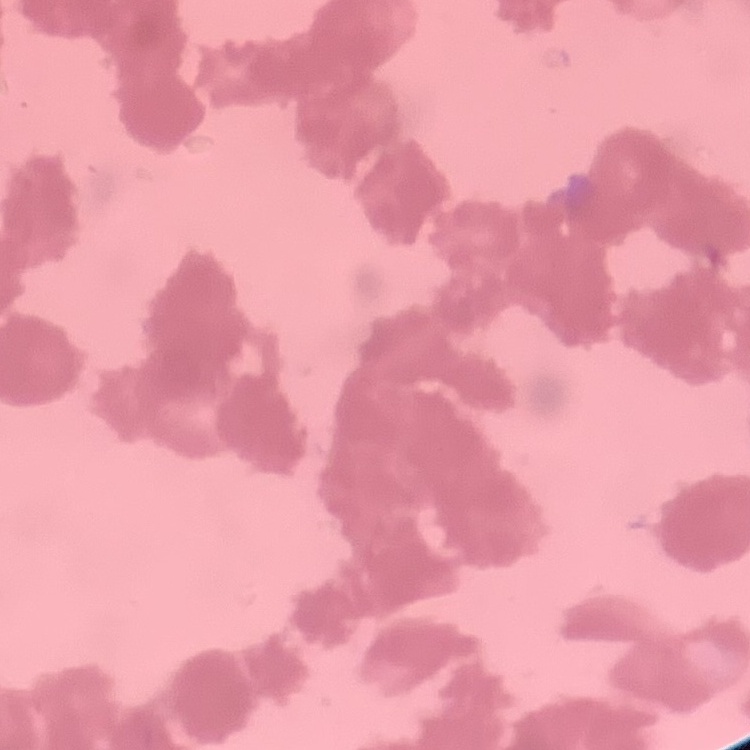
erythrocyte_morphology: rouleaux formation
image_type: square crop of a larger photomicrograph
stain: Field's or Giemsa
preparation: thin blood smear